Describe the morphology of the erythrocytes.
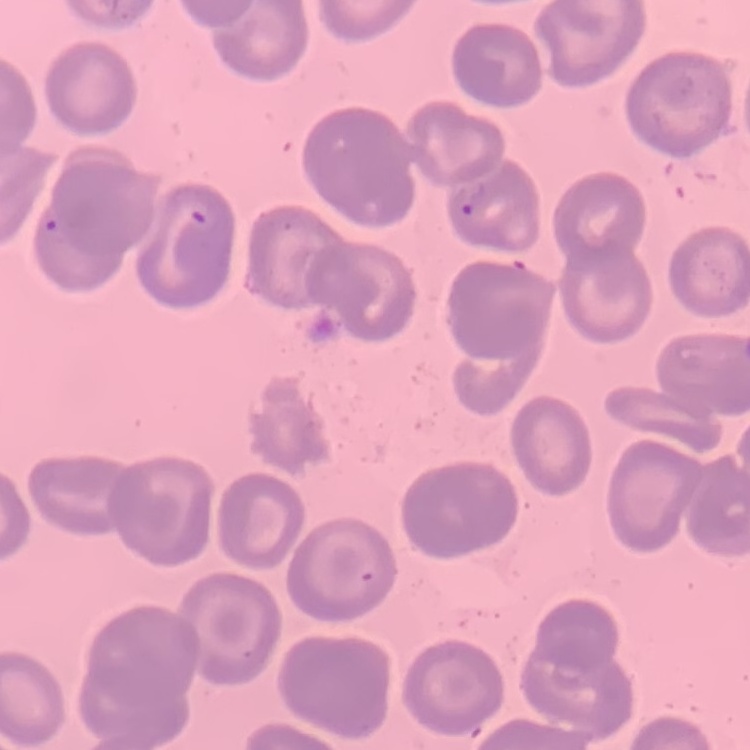
They show no rouleaux formation.

{
  "preparation": "thin blood smear",
  "stain": "Field's or Giemsa",
  "image_type": "square crop of a larger photomicrograph"
}